State which parasite is depicted.
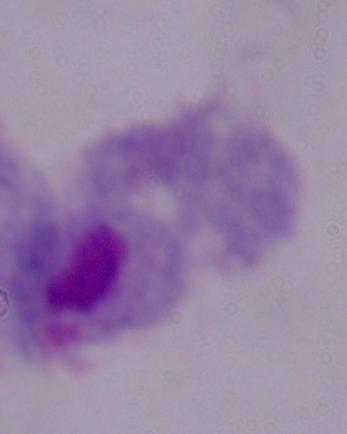

A trichomonad.

Summary:
  - Magnification: 1000x
  - Modality: micrograph